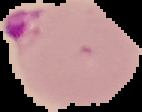

Image is 142×112 pixels. Malaria status: parasitized. The area outside the segmented cell region is set to black. From a thin blood film.